Locate every Plasmodium parasite.
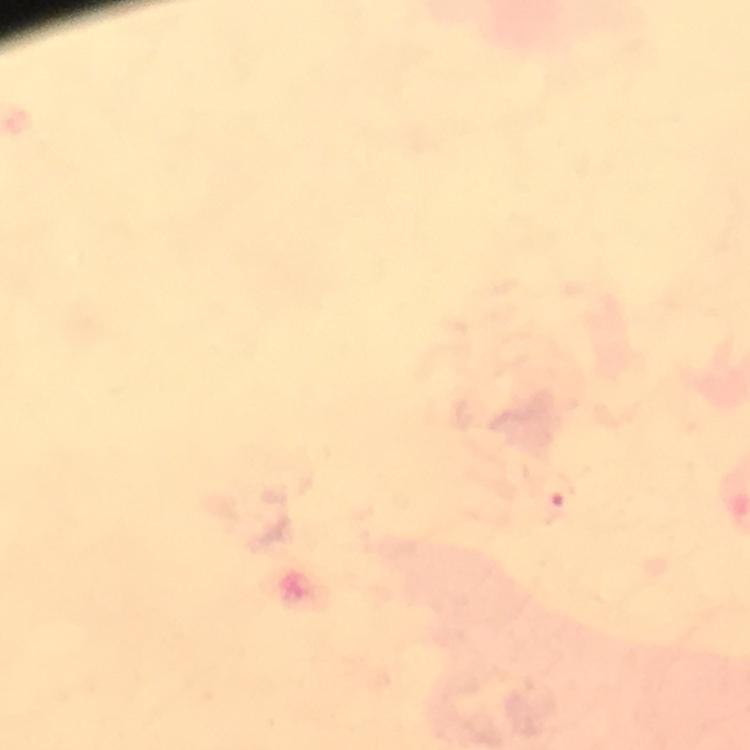

Approximate centers as [x, y] in pixels.
Plasmodium parasites: [555, 498].

Giemsa-stained preparation. Thick blood smear. 100x magnification. From a malaria diagnostic workup. Image is 750×750 pixels. Immersion oil was used. Photographed with a smartphone mounted on the microscope. Cropped region of a single field of view.